Assess this cell for malaria.
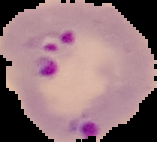
It is parasitized.

Summary:
  - Image size: 157×142 pixels
  - Preparation: thin blood film
  - Image type: cell region segmented out of the field of view; surrounding area masked to black